Describe the morphology of the red blood cells.
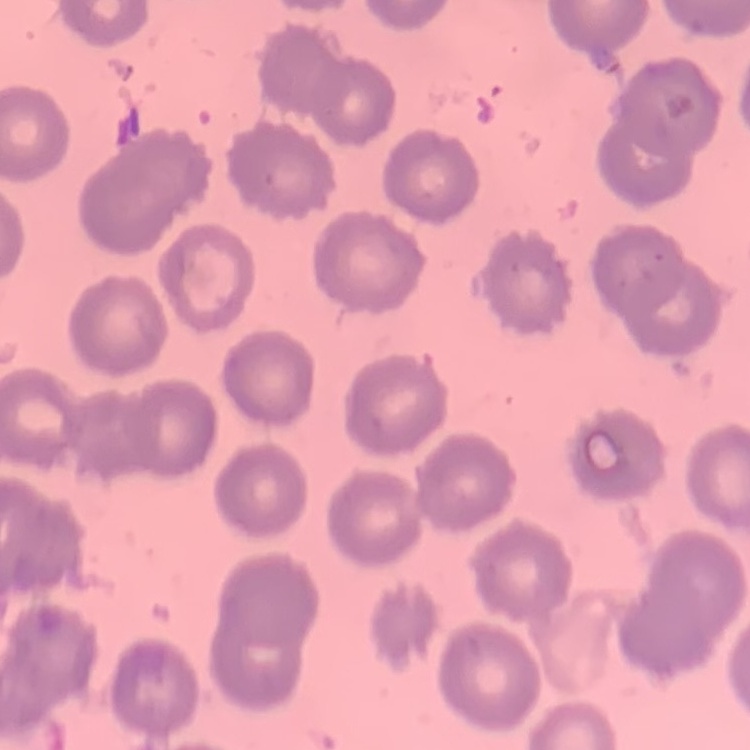
No rouleaux formation.

Thin blood film. One tile cut from a larger photomicrograph. Field's or Giemsa stain.